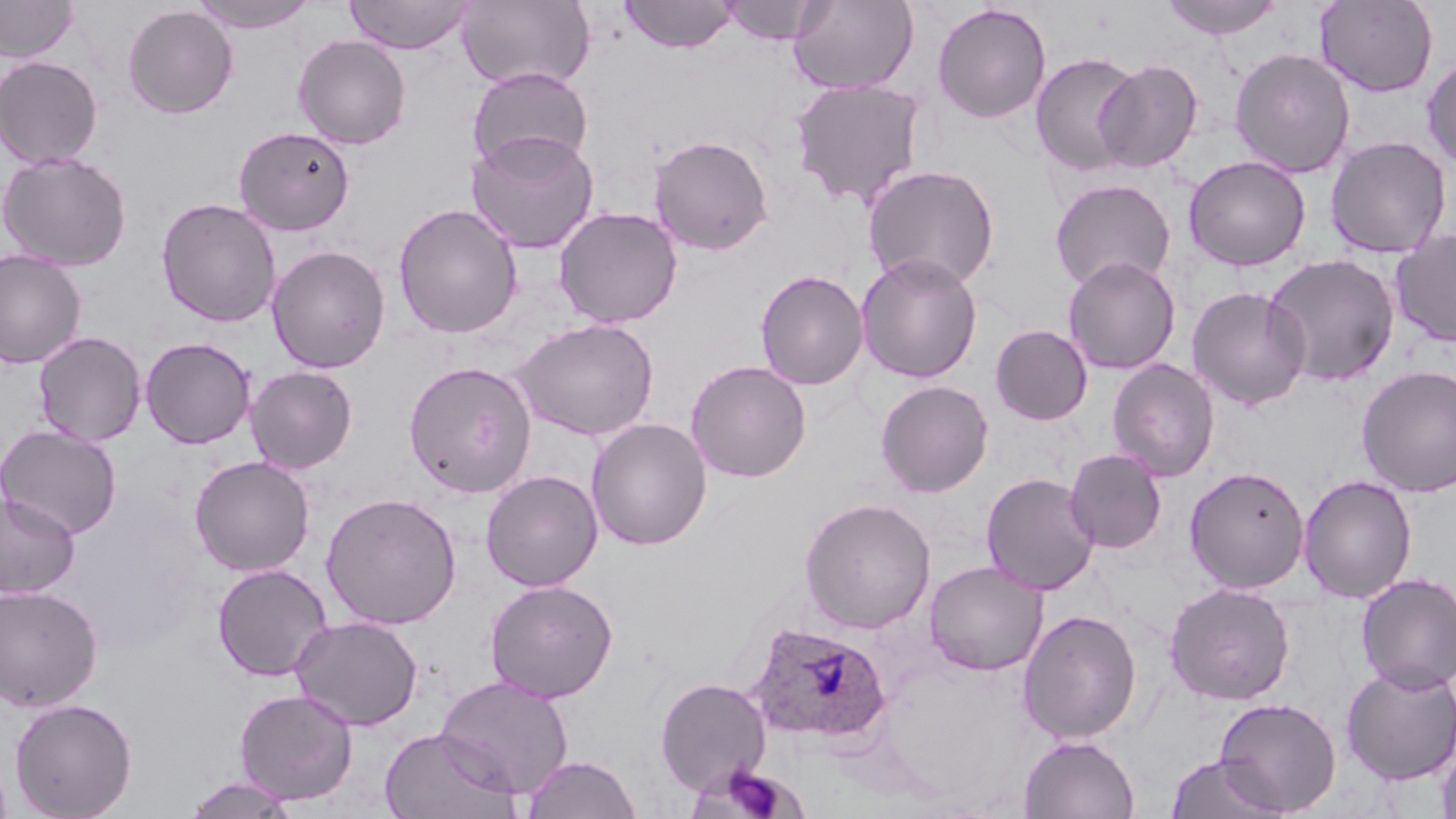

Summary:
  - Coordinate format: approximate bounding boxes as named x1/y1/x2/y2 corners in pixels
  - Plasmodium ovale-infected red blood cell locations: (x1=746, y1=620, x2=891, y2=744)
  - Uninfected red blood cell locations: (x1=0, y1=0, x2=79, y2=63), (x1=344, y1=0, x2=475, y2=54), (x1=456, y1=0, x2=596, y2=92), (x1=620, y1=0, x2=738, y2=54), (x1=718, y1=0, x2=829, y2=45), (x1=788, y1=0, x2=919, y2=95), (x1=1158, y1=0, x2=1285, y2=39), (x1=1314, y1=0, x2=1439, y2=97), (x1=187, y1=1, x2=320, y2=34), (x1=932, y1=3, x2=1051, y2=123), (x1=122, y1=4, x2=238, y2=119), (x1=293, y1=34, x2=411, y2=149), (x1=1229, y1=48, x2=1356, y2=179), (x1=1030, y1=53, x2=1142, y2=176), (x1=1421, y1=54, x2=1456, y2=171), (x1=0, y1=55, x2=104, y2=170), (x1=1094, y1=59, x2=1202, y2=173), (x1=466, y1=67, x2=593, y2=172), (x1=790, y1=77, x2=926, y2=210), (x1=233, y1=125, x2=356, y2=235), (x1=466, y1=129, x2=599, y2=254), (x1=648, y1=134, x2=774, y2=256), (x1=1325, y1=135, x2=1452, y2=259), (x1=0, y1=151, x2=132, y2=271), (x1=1184, y1=155, x2=1311, y2=271), (x1=862, y1=163, x2=1000, y2=290), (x1=1049, y1=178, x2=1176, y2=292), (x1=156, y1=197, x2=282, y2=328), (x1=393, y1=202, x2=523, y2=339), (x1=554, y1=206, x2=683, y2=328), (x1=1390, y1=228, x2=1456, y2=348), (x1=266, y1=244, x2=391, y2=374), (x1=0, y1=250, x2=87, y2=369), (x1=856, y1=252, x2=983, y2=384), (x1=1263, y1=253, x2=1401, y2=387), (x1=1063, y1=256, x2=1181, y2=375), (x1=754, y1=269, x2=869, y2=390), (x1=1187, y1=286, x2=1312, y2=411), (x1=513, y1=317, x2=659, y2=441), (x1=989, y1=324, x2=1093, y2=425), (x1=33, y1=330, x2=147, y2=446), (x1=140, y1=336, x2=256, y2=449), (x1=685, y1=359, x2=812, y2=483), (x1=1107, y1=359, x2=1220, y2=482), (x1=404, y1=360, x2=537, y2=498), (x1=245, y1=365, x2=358, y2=474), (x1=1357, y1=365, x2=1456, y2=497), (x1=875, y1=380, x2=994, y2=498), (x1=586, y1=418, x2=712, y2=550), (x1=0, y1=424, x2=123, y2=539), (x1=1065, y1=448, x2=1167, y2=553), (x1=190, y1=455, x2=315, y2=576), (x1=1184, y1=466, x2=1310, y2=594), (x1=480, y1=469, x2=603, y2=592), (x1=980, y1=471, x2=1101, y2=596), (x1=1298, y1=474, x2=1418, y2=603), (x1=0, y1=492, x2=81, y2=599), (x1=321, y1=492, x2=463, y2=630), (x1=799, y1=497, x2=937, y2=635), (x1=924, y1=560, x2=1048, y2=676), (x1=211, y1=563, x2=334, y2=682), (x1=1355, y1=572, x2=1456, y2=693), (x1=484, y1=579, x2=618, y2=703), (x1=1165, y1=582, x2=1296, y2=705), (x1=0, y1=584, x2=104, y2=712), (x1=1018, y1=609, x2=1142, y2=744), (x1=289, y1=615, x2=424, y2=731), (x1=1340, y1=663, x2=1456, y2=785), (x1=435, y1=676, x2=574, y2=799), (x1=654, y1=677, x2=772, y2=796), (x1=234, y1=689, x2=359, y2=804), (x1=9, y1=697, x2=138, y2=819), (x1=1214, y1=697, x2=1342, y2=815), (x1=379, y1=728, x2=520, y2=819), (x1=1019, y1=735, x2=1140, y2=819), (x1=1437, y1=739, x2=1456, y2=819), (x1=522, y1=755, x2=642, y2=818), (x1=1165, y1=755, x2=1286, y2=819), (x1=184, y1=776, x2=301, y2=818)
  - Slide-level diagnosis: Plasmodium ovale
  - Magnification: 1000x
  - Preparation: thin blood smear
  - Image size: 1456×819 pixels
  - Stain: May-Grünwald-Giemsa
  - Modality: light microscopy
  - Field of view: one of a larger specimen